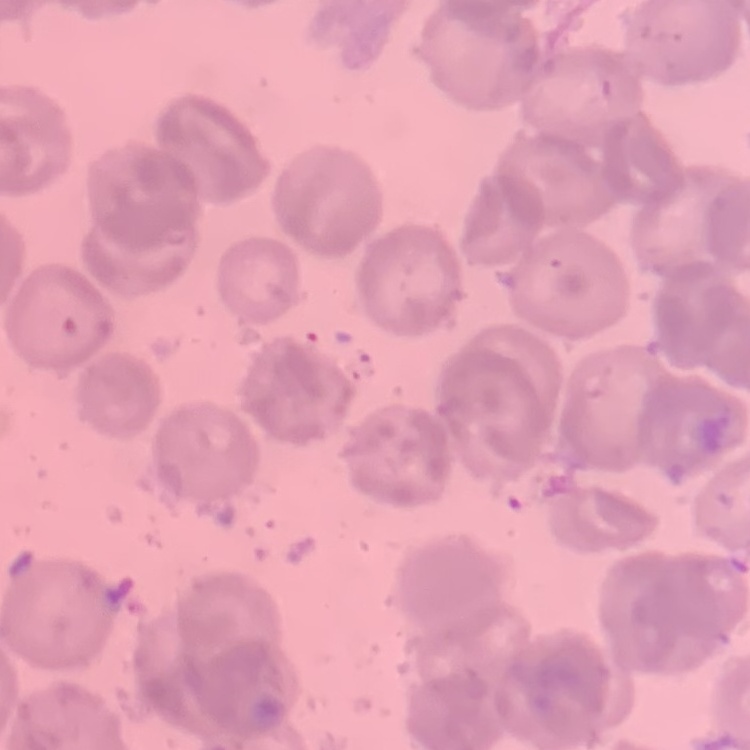

Summary:
  - Red blood cell morphology: no rouleaux formation
  - Preparation: thin peripheral smear
  - Stain: Field's or Giemsa
  - Image type: square crop of a larger photomicrograph